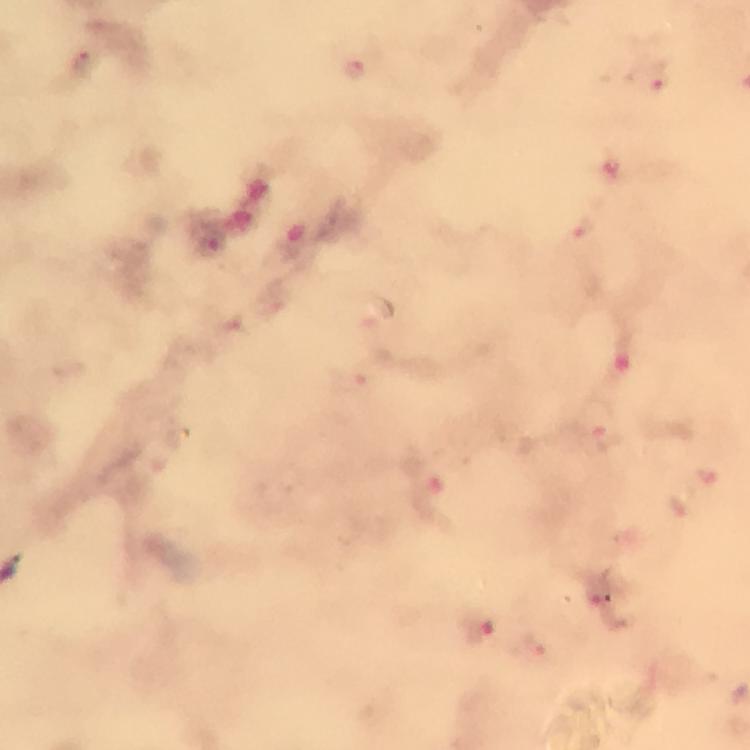

capture = smartphone camera through the microscope
immersion oil = used
cropped from = one field of view
image size = 750×750 pixels
malaria parasite locations = approximate object centers, in pixels from the top-left corner: (x=354, y=70), (x=657, y=78), (x=607, y=436), (x=479, y=626), (x=536, y=647)
preparation = thick blood smear
magnification = 100x
context = from a malaria diagnostic workup
stain = Giemsa